Comment on the morphology of the red blood cells.
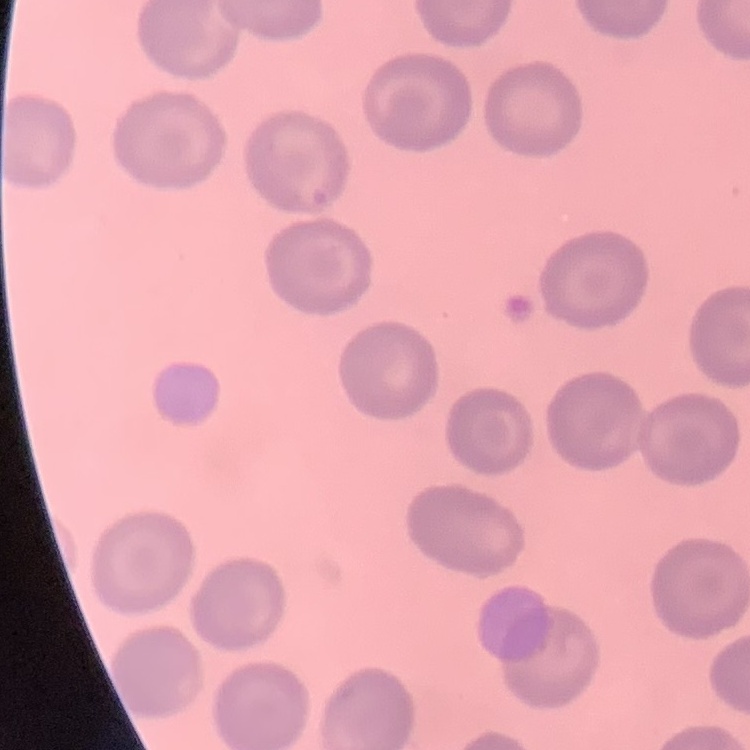

They show no rouleaux formation.

stain: Field's or Giemsa
preparation: thin blood film
image_type: one tile cut from a larger photomicrograph